Give the position of every Plasmodium parasite and every leukocyte.
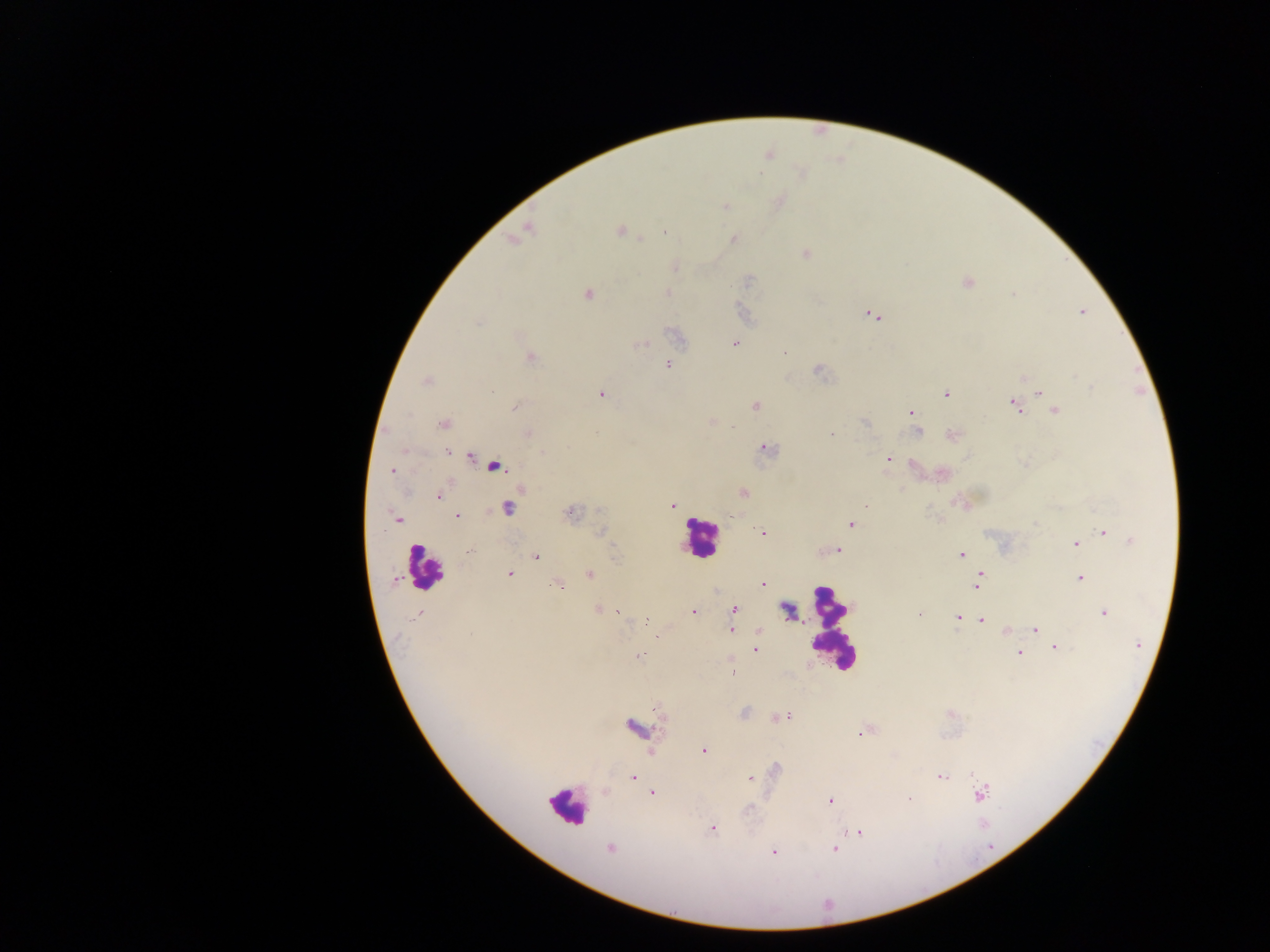

Approximate centers as [x, y] in pixels.
Plasmodium parasites: [724, 208], [622, 230], [663, 233], [734, 240], [804, 252], [750, 280], [966, 283], [589, 294], [1083, 312], [869, 314], [876, 319], [478, 322], [648, 344], [735, 344], [638, 346], [782, 352], [528, 357], [668, 366], [820, 371], [1023, 377], [1075, 378], [425, 383], [1091, 385], [1039, 392], [599, 393], [945, 393], [1012, 404], [754, 406], [515, 407], [1056, 410], [910, 412], [710, 421], [865, 422], [443, 424], [735, 425], [918, 432], [831, 434], [950, 434], [767, 448], [403, 449], [448, 451], [472, 457], [888, 457], [914, 463], [495, 467], [392, 472], [743, 493], [440, 498], [672, 504], [866, 504], [929, 509], [508, 510], [571, 514], [457, 517], [399, 519], [852, 525], [1104, 532], [601, 533], [763, 533], [1130, 541], [1074, 543], [837, 550], [468, 551], [961, 555], [536, 557], [589, 575], [511, 576], [979, 576], [1081, 577], [394, 580], [764, 584], [558, 586], [977, 589], [596, 609], [604, 609], [733, 609], [692, 612], [1103, 612], [617, 613], [918, 613], [419, 614], [957, 615], [646, 620], [982, 622], [1035, 629], [732, 630], [759, 631], [1006, 632], [471, 634], [655, 637], [1136, 645], [1053, 646], [756, 648], [1019, 653], [639, 655], [787, 715], [776, 718], [633, 727], [859, 734], [704, 752], [941, 776], [633, 778], [751, 779], [654, 792], [980, 794], [910, 798], [830, 801], [712, 829], [862, 832], [835, 849], [610, 850], [772, 851].
Leukocytes: [703, 545], [423, 570], [831, 628], [570, 805].

Summary:
  - Field of view: single
  - Capture: mobile-phone photograph through a microscope
  - Country: Ghana
  - Preparation: thick blood smear
  - Image size: 1270×952 pixels